Outline each blood parasite and name the species.
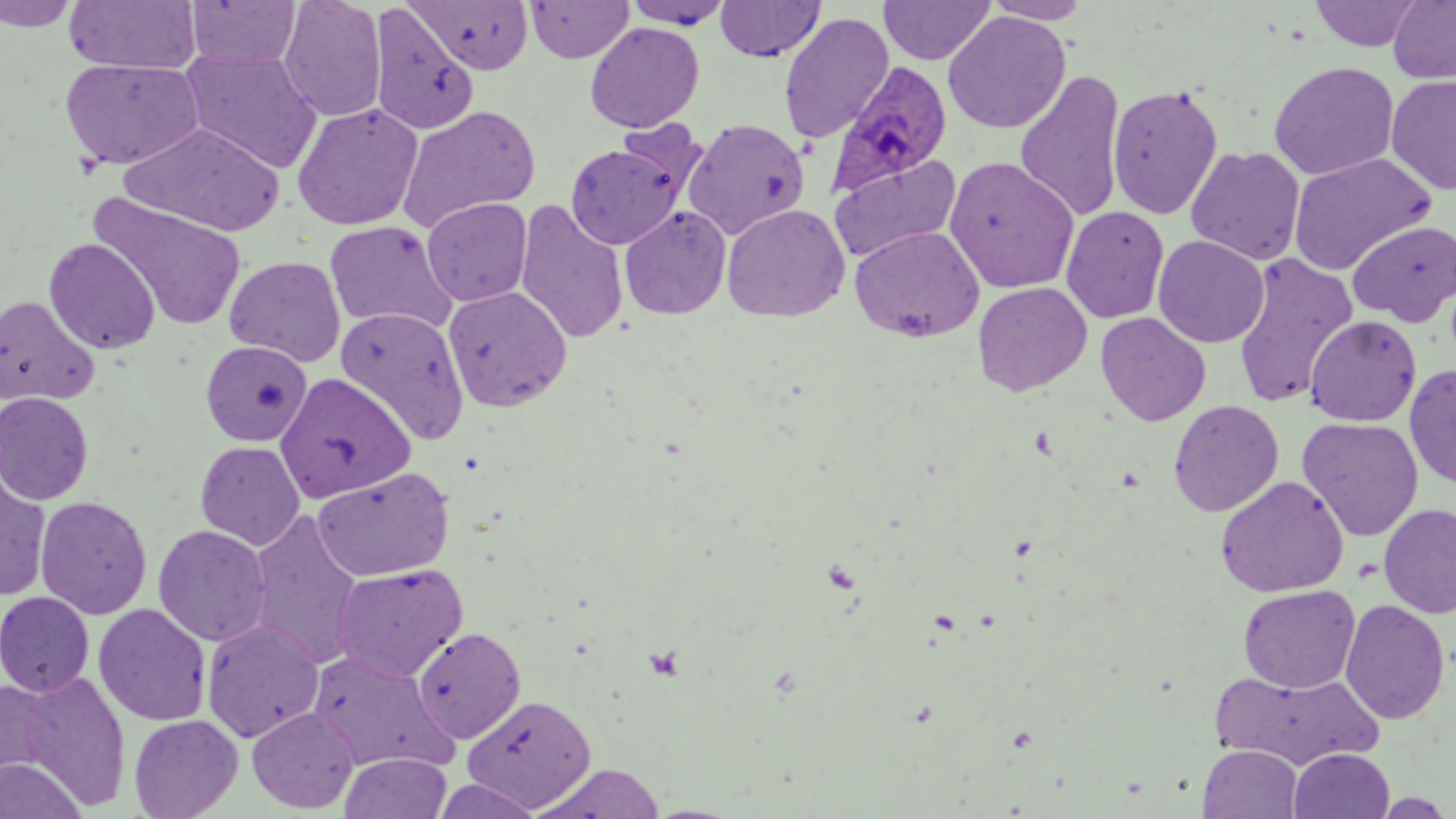

Approximate bounding boxes as [x1, y1, x2, y2] in pixels.
Plasmodium ovale-infected red blood cells: [829, 62, 953, 194].
No Plasmodium falciparum, Plasmodium malariae, Plasmodium vivax, Babesia divergens, or Trypanosoma brucei observed.

Uninfected red blood cell locations: [184, 0, 302, 69], [278, 0, 387, 122], [408, 0, 534, 74], [526, 0, 634, 63], [621, 0, 736, 29], [982, 0, 1093, 24], [1310, 0, 1426, 52], [1388, 0, 1455, 85], [0, 1, 82, 31], [63, 1, 202, 74], [715, 1, 825, 61], [878, 1, 996, 66], [369, 4, 479, 136], [943, 11, 1071, 134], [778, 12, 894, 144], [585, 22, 704, 133], [180, 49, 322, 173], [60, 57, 204, 170], [1268, 61, 1400, 181], [1014, 71, 1127, 222], [1386, 74, 1456, 194], [1107, 84, 1223, 220], [291, 102, 424, 231], [397, 105, 541, 232], [683, 118, 809, 239], [613, 119, 710, 203], [119, 122, 286, 236], [565, 141, 686, 249], [1186, 145, 1305, 265], [829, 152, 962, 265], [1288, 152, 1437, 276], [945, 156, 1080, 294], [89, 193, 248, 332], [421, 197, 533, 307], [514, 200, 629, 345], [721, 203, 849, 322], [620, 205, 731, 320], [1061, 205, 1169, 324], [1347, 219, 1456, 327], [324, 220, 458, 336], [850, 225, 984, 342], [1153, 235, 1270, 348], [44, 238, 161, 355], [1231, 252, 1358, 408], [223, 255, 346, 366], [972, 281, 1093, 396], [443, 286, 572, 412], [0, 295, 99, 407], [336, 307, 470, 443], [1096, 311, 1211, 426], [1305, 314, 1422, 426], [200, 340, 313, 446], [1404, 363, 1456, 489], [275, 373, 416, 502], [0, 392, 94, 504], [1168, 399, 1285, 517], [1298, 416, 1424, 541], [195, 441, 305, 549], [177, 456, 310, 619], [0, 457, 52, 602], [312, 467, 454, 581], [1216, 475, 1349, 597], [35, 495, 152, 619], [1378, 503, 1456, 618], [246, 511, 365, 669], [152, 524, 271, 646], [331, 563, 467, 681], [1238, 584, 1360, 693], [0, 591, 95, 697], [1340, 599, 1451, 725], [93, 603, 211, 726], [202, 619, 324, 742], [412, 626, 527, 744], [306, 650, 455, 774], [1211, 668, 1383, 770], [16, 669, 131, 811], [1, 677, 58, 783], [462, 694, 596, 812], [247, 706, 359, 813], [128, 713, 243, 819], [1198, 744, 1303, 819], [1288, 748, 1395, 819], [339, 753, 452, 819], [0, 756, 87, 819], [532, 763, 667, 819], [431, 777, 543, 819]. Slide-level diagnosis: Plasmodium ovale. Single field of view. Thin blood smear. Image is 1456×819 pixels. Optical microscopy. May-Grünwald-Giemsa stain. 1000x magnification.